Point out each Plasmodium parasite.
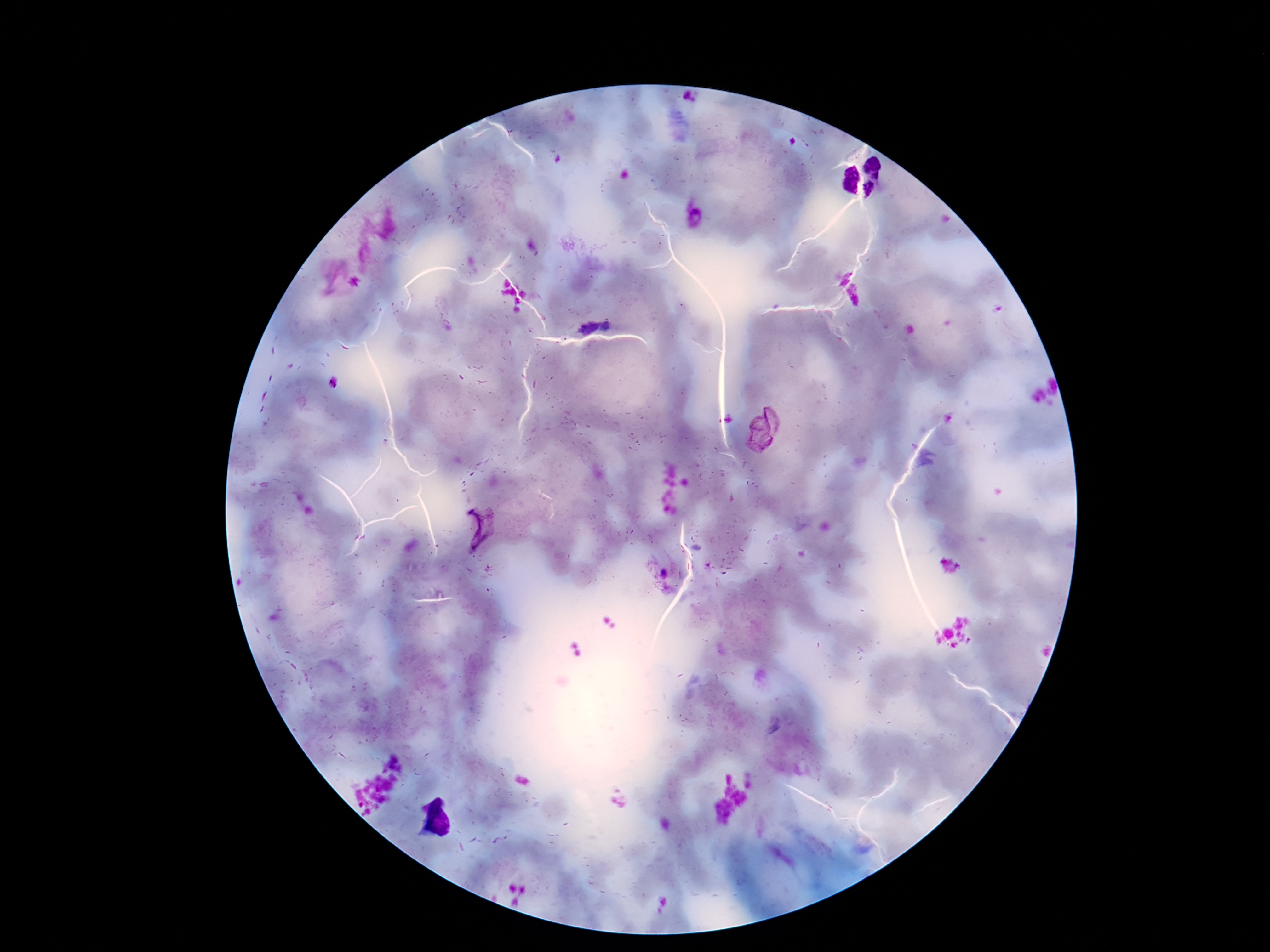

Approximate centers as [x, y] in pixels.
Plasmodium parasites: [840, 275], [855, 295], [595, 325], [762, 431], [479, 526].

Summary:
  - Capture: smartphone camera through the microscope eyepiece
  - Stain: Giemsa
  - Field of view: single
  - Image size: 1270×952 pixels
  - Magnification: 100x
  - Patient malaria status: positive
  - Preparation: thick peripheral-blood smear